Name the parasite shown.
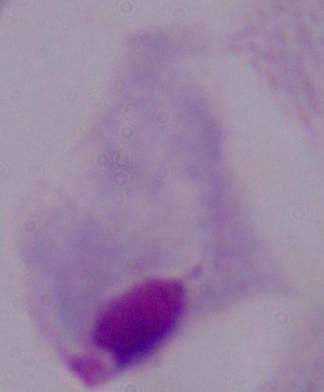
A trichomonad.

{
  "magnification": "1000x",
  "modality": "photomicrograph"
}